Report the malaria status of this cell.
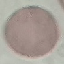

It is uninfected.

Summary:
  - Preparation: thin smear
  - Stain: Giemsa
  - Capture: smartphone camera at the microscope eyepiece
  - Image type: automatically extracted cell patch, resized to 64 × 64 pixels